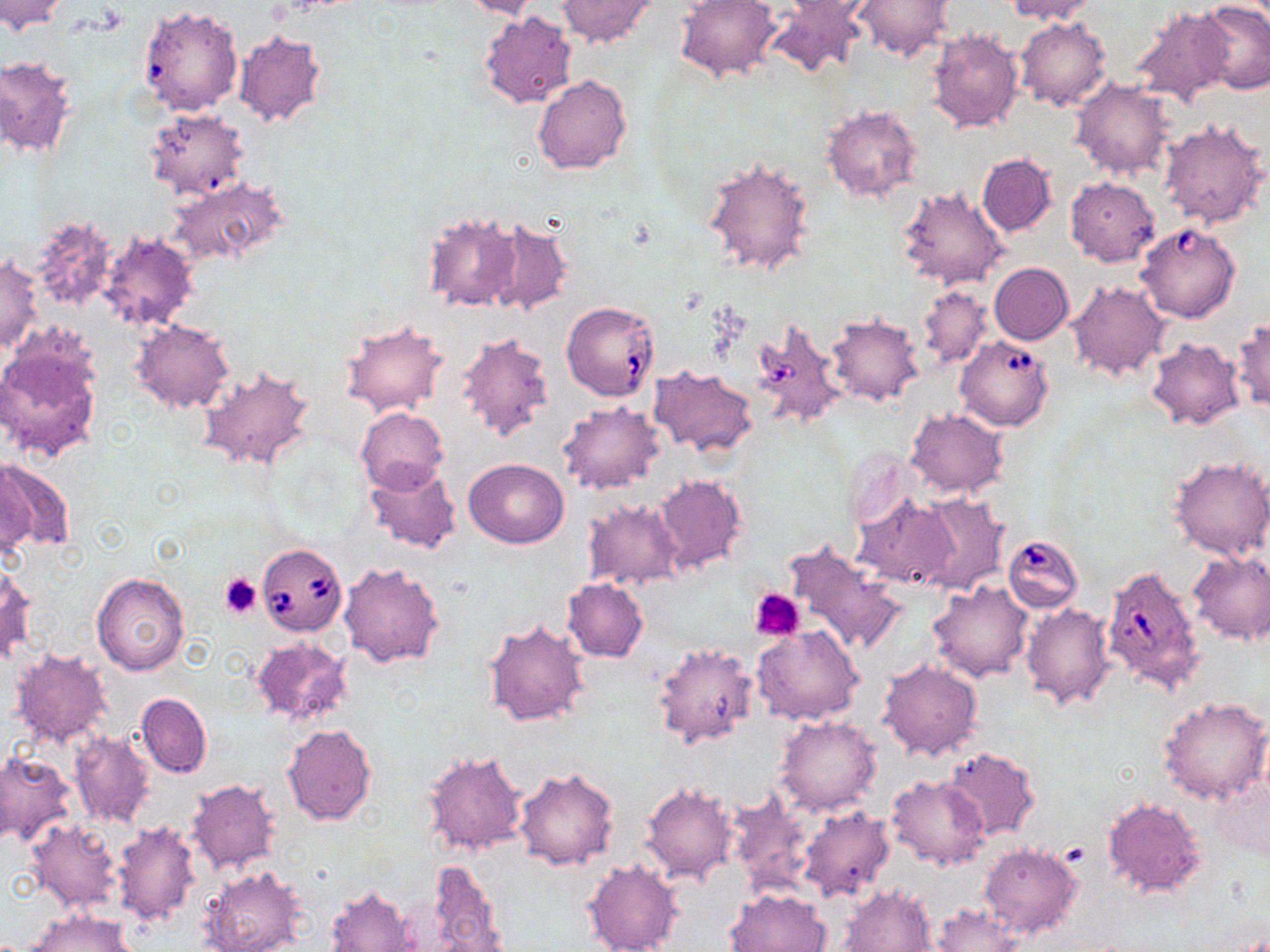
Approximate bounding boxes as named x1/y1/x2/y2 corners in pixels. Platelet locations: (x1=220, y1=573, x2=262, y2=618), (x1=750, y1=587, x2=806, y2=640). Uninfected red blood cell locations: (x1=0, y1=0, x2=68, y2=34), (x1=674, y1=0, x2=781, y2=84), (x1=787, y1=0, x2=875, y2=22), (x1=1004, y1=0, x2=1098, y2=23), (x1=459, y1=1, x2=542, y2=20), (x1=555, y1=1, x2=660, y2=49), (x1=766, y1=1, x2=866, y2=78), (x1=853, y1=1, x2=952, y2=62), (x1=1194, y1=3, x2=1270, y2=93), (x1=138, y1=5, x2=243, y2=117), (x1=1128, y1=7, x2=1234, y2=106), (x1=480, y1=9, x2=578, y2=108), (x1=1015, y1=15, x2=1112, y2=111), (x1=927, y1=27, x2=1023, y2=135), (x1=233, y1=30, x2=326, y2=127), (x1=1, y1=55, x2=76, y2=158), (x1=532, y1=74, x2=633, y2=174), (x1=1070, y1=77, x2=1175, y2=180), (x1=820, y1=105, x2=923, y2=203), (x1=143, y1=108, x2=250, y2=200), (x1=1159, y1=116, x2=1268, y2=229), (x1=977, y1=153, x2=1056, y2=236), (x1=702, y1=154, x2=816, y2=278), (x1=171, y1=177, x2=289, y2=269), (x1=1065, y1=177, x2=1160, y2=266), (x1=896, y1=185, x2=1009, y2=291), (x1=421, y1=209, x2=524, y2=313), (x1=25, y1=214, x2=120, y2=313), (x1=483, y1=214, x2=574, y2=316), (x1=98, y1=231, x2=201, y2=331), (x1=1, y1=255, x2=42, y2=355), (x1=989, y1=262, x2=1073, y2=344), (x1=1068, y1=280, x2=1168, y2=380), (x1=917, y1=285, x2=991, y2=370), (x1=827, y1=312, x2=924, y2=406), (x1=1231, y1=316, x2=1269, y2=412), (x1=340, y1=318, x2=449, y2=418), (x1=132, y1=319, x2=234, y2=413), (x1=455, y1=332, x2=554, y2=444), (x1=1146, y1=336, x2=1245, y2=430), (x1=0, y1=346, x2=102, y2=463), (x1=196, y1=365, x2=318, y2=474), (x1=650, y1=366, x2=758, y2=456), (x1=557, y1=401, x2=665, y2=495), (x1=356, y1=406, x2=448, y2=494), (x1=905, y1=407, x2=1009, y2=499), (x1=842, y1=445, x2=917, y2=530), (x1=1168, y1=455, x2=1270, y2=560), (x1=463, y1=458, x2=569, y2=548), (x1=1, y1=459, x2=74, y2=553), (x1=0, y1=462, x2=34, y2=562), (x1=364, y1=463, x2=461, y2=555), (x1=653, y1=474, x2=748, y2=574), (x1=916, y1=493, x2=1007, y2=594), (x1=853, y1=494, x2=958, y2=588), (x1=582, y1=498, x2=684, y2=591), (x1=783, y1=540, x2=908, y2=656), (x1=1188, y1=551, x2=1270, y2=645), (x1=338, y1=561, x2=444, y2=667), (x1=0, y1=563, x2=36, y2=664), (x1=91, y1=572, x2=189, y2=676), (x1=562, y1=577, x2=648, y2=662), (x1=927, y1=581, x2=1033, y2=682), (x1=1021, y1=601, x2=1116, y2=709), (x1=482, y1=618, x2=590, y2=728), (x1=752, y1=626, x2=863, y2=726), (x1=251, y1=635, x2=353, y2=726), (x1=652, y1=642, x2=759, y2=749), (x1=9, y1=646, x2=113, y2=750), (x1=877, y1=659, x2=983, y2=761), (x1=136, y1=692, x2=212, y2=778), (x1=1159, y1=696, x2=1270, y2=805), (x1=774, y1=714, x2=883, y2=817), (x1=281, y1=724, x2=377, y2=824), (x1=70, y1=731, x2=154, y2=827), (x1=942, y1=746, x2=1040, y2=840), (x1=421, y1=748, x2=527, y2=858), (x1=0, y1=750, x2=77, y2=847), (x1=1212, y1=764, x2=1270, y2=863), (x1=513, y1=766, x2=619, y2=871), (x1=886, y1=774, x2=992, y2=869), (x1=184, y1=779, x2=281, y2=874), (x1=639, y1=779, x2=740, y2=886), (x1=729, y1=787, x2=814, y2=896), (x1=1101, y1=796, x2=1206, y2=899), (x1=797, y1=806, x2=895, y2=903), (x1=25, y1=818, x2=123, y2=914), (x1=113, y1=819, x2=201, y2=928), (x1=979, y1=842, x2=1084, y2=940), (x1=580, y1=858, x2=684, y2=952), (x1=417, y1=859, x2=505, y2=952), (x1=199, y1=865, x2=305, y2=952), (x1=838, y1=882, x2=938, y2=952), (x1=324, y1=885, x2=420, y2=951), (x1=725, y1=888, x2=831, y2=952), (x1=929, y1=903, x2=1023, y2=952), (x1=27, y1=909, x2=137, y2=952). Babesia divergens-infected red blood cell locations: (x1=1135, y1=222, x2=1241, y2=323), (x1=562, y1=301, x2=662, y2=401), (x1=751, y1=318, x2=846, y2=429), (x1=954, y1=336, x2=1054, y2=431), (x1=1008, y1=532, x2=1082, y2=610), (x1=256, y1=543, x2=348, y2=636), (x1=1102, y1=562, x2=1205, y2=694). Slide-level diagnosis: Babesia divergens. Image is 1270×952 pixels. Optical microscopy. Thin blood film. Captured at 1000x magnification. Single field of view. May-Grünwald-Giemsa stain.